Comment on the morphology of the red blood cells.
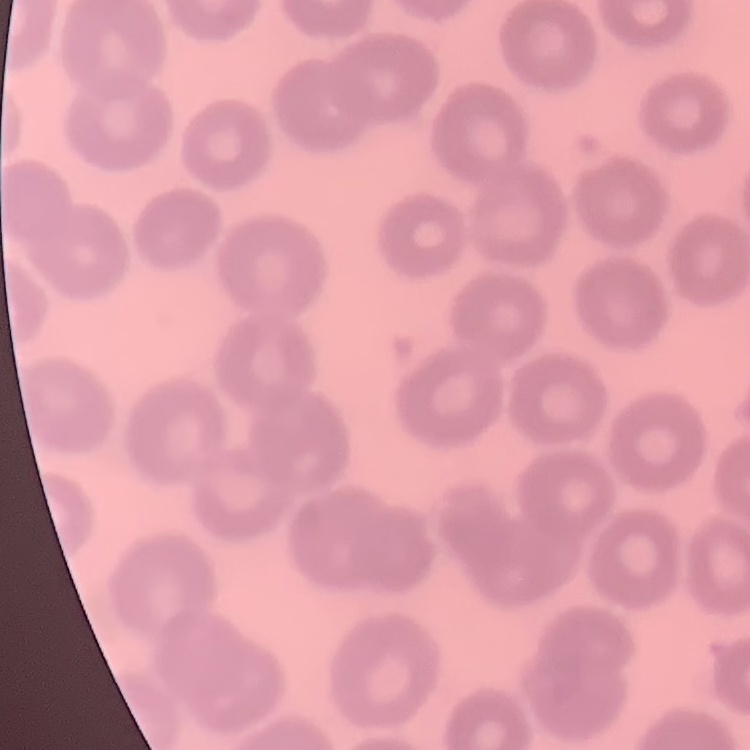
They show no rouleaux formation.

Thin blood smear. Field's or Giemsa stain. One tile cut from a larger photomicrograph.